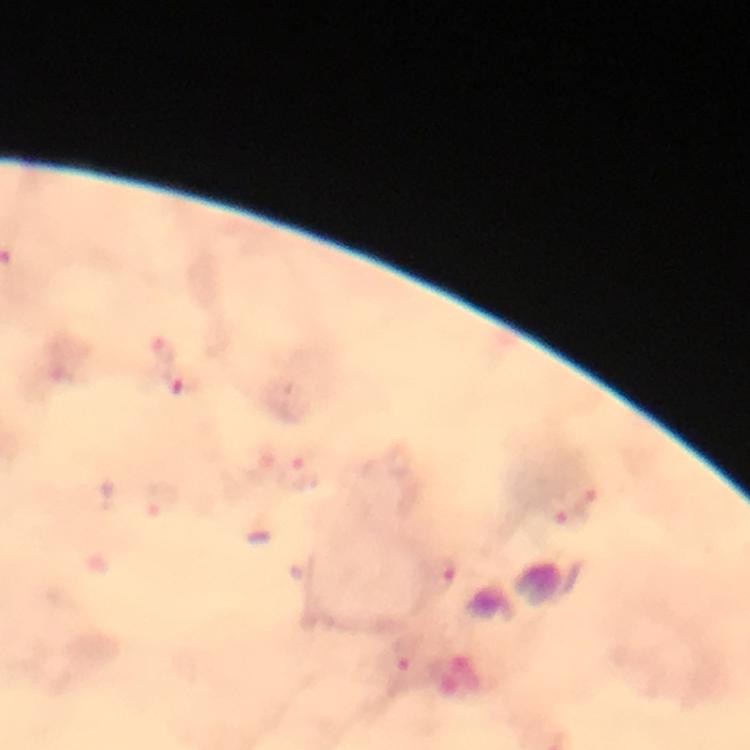
Approximate centers as [x, y] in pixels. Plasmodium parasite locations: [183, 383]. Thick smear. At 100x magnification. From a diagnostic examination for malaria. Giemsa stain. Photographed through the microscope with a smartphone camera. Cropped region of a single field of view. Immersion oil was used. Image is 750×750 pixels.